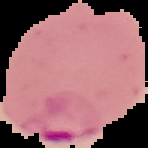
From a thin blood film. Image is 148×148 pixels. Malaria status: parasitized. Cell region segmented out of the field of view; the surrounding area is masked to black.